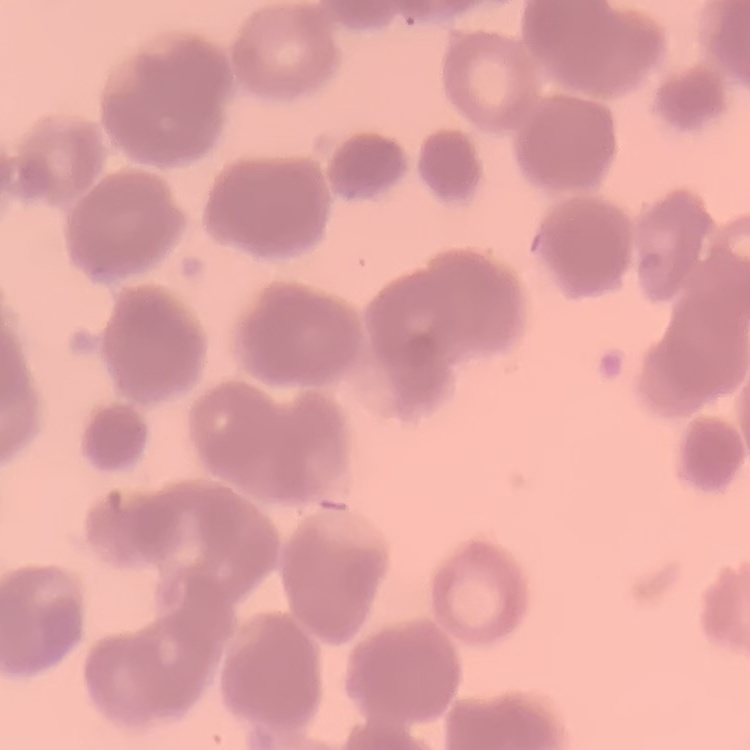 The erythrocytes show rouleaux formation. Field's or Giemsa stain. One tile cut from a larger photomicrograph. Thin blood film.